Point out each Plasmodium parasite.
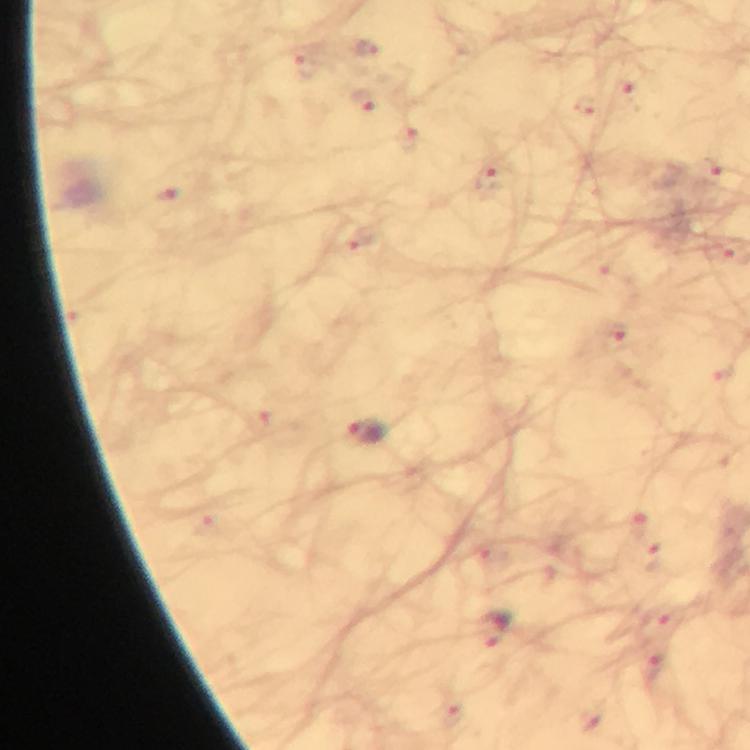
Approximate centers as [x, y] in pixels.
Plasmodium parasites: [367, 432], [494, 630].

From a malaria diagnostic workup. Giemsa-stained preparation. Image is 750×750 pixels. At 100x magnification. Photographed with a smartphone mounted on the microscope. Immersion oil applied. Cropped region of a single field of view. Thick blood film.